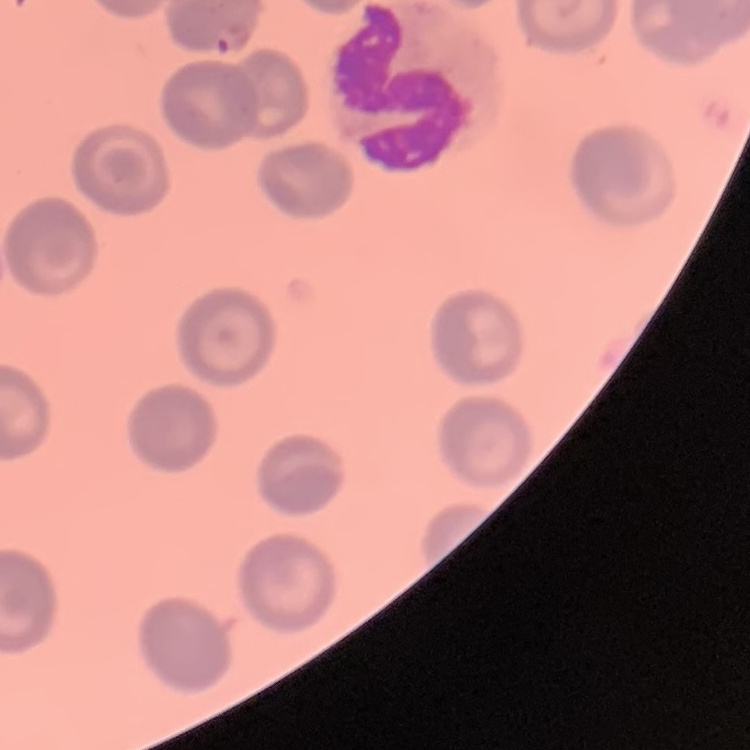
erythrocyte morphology = no rouleaux formation
stain = Field's or Giemsa
image type = one tile cut from a larger photomicrograph
preparation = thin peripheral smear